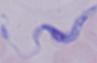
A trypanosome is shown. Captured at 1000x magnification. Photomicrograph.